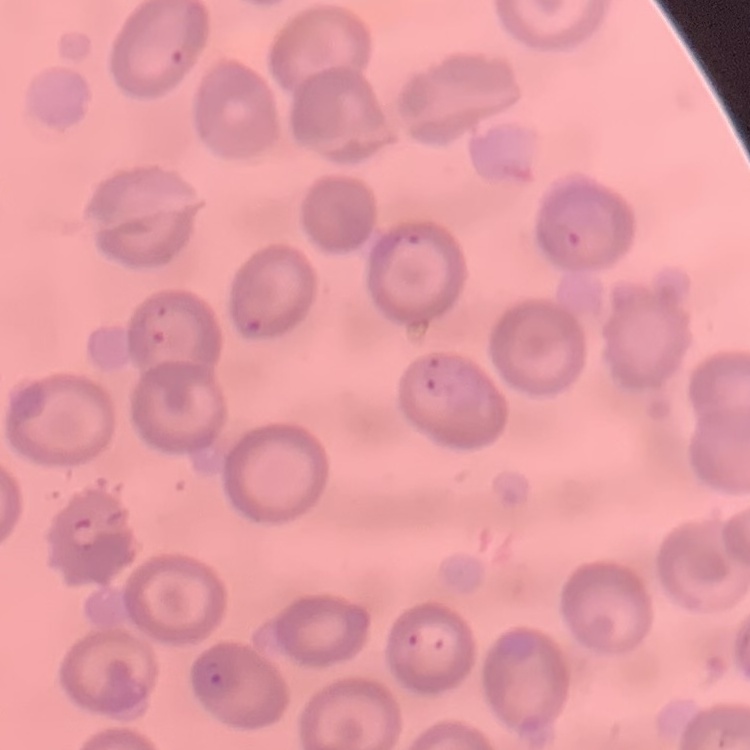

Summary:
  - Red blood cell morphology: no rouleaux formation
  - Image type: one tile cut from a larger photomicrograph
  - Preparation: thin blood smear
  - Stain: Field's or Giemsa